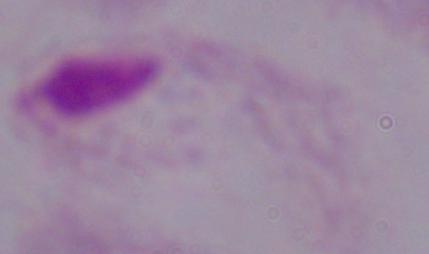

{
  "magnification": "1000x",
  "identification": "trichomonad",
  "modality": "micrograph"
}